Assess this cell for malaria.
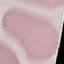
Uninfected.

Photographed with a smartphone camera at the microscope eyepiece. Cell patch, automatically extracted from a larger field of view and resized to 64 × 64 pixels. Thin blood film. Giemsa stain.